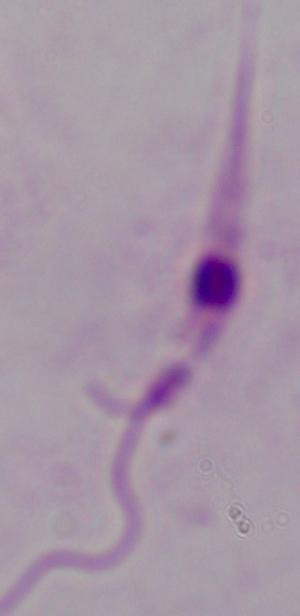
identification: Leishmania
modality: photomicrograph
magnification: 1000x